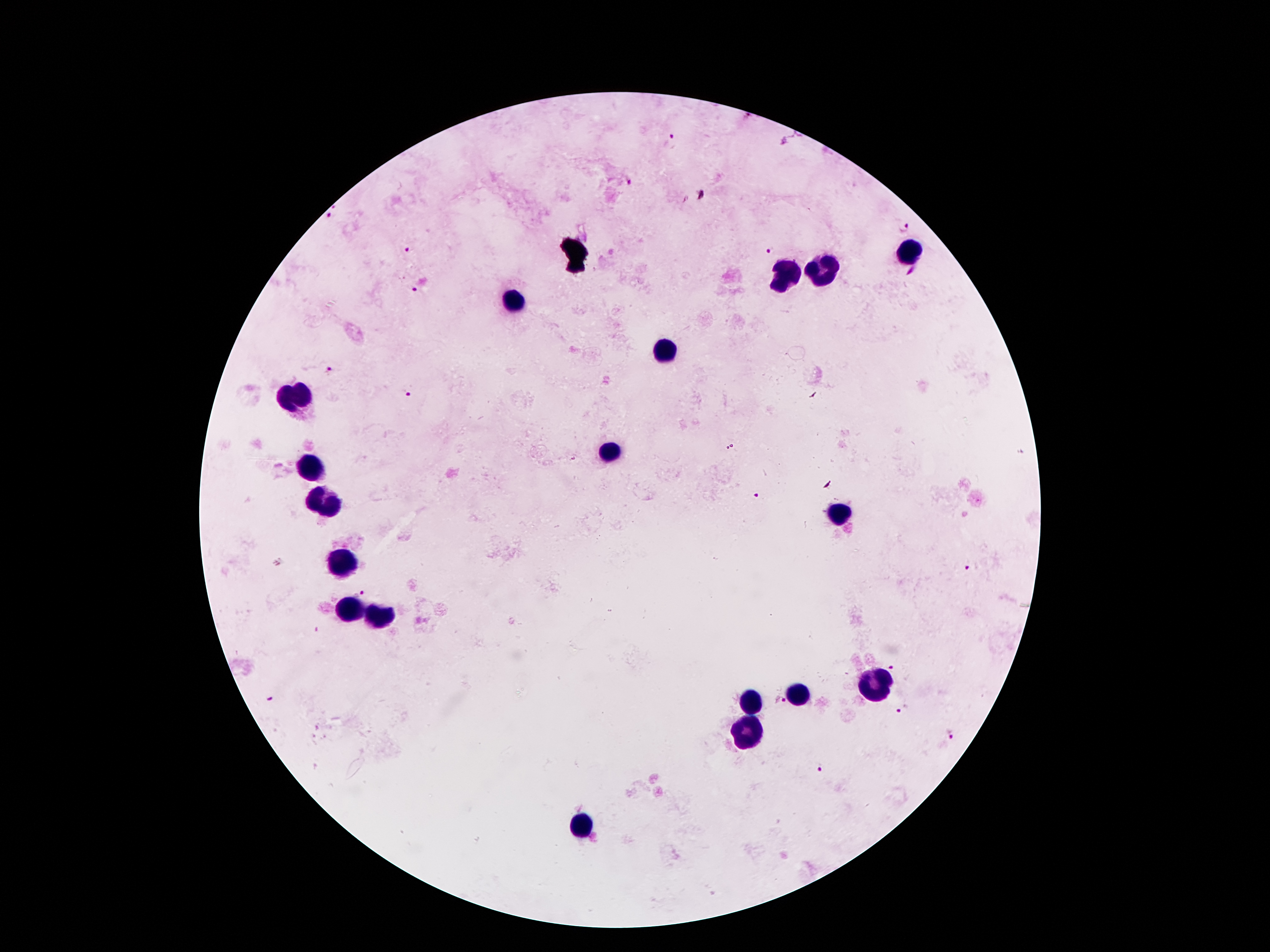

image_size: 1270×952 pixels
leukocyte_locations: 'approximate centers as [x, y] in pixels: [905, 250], [823, 272], [787, 275], [515, 298], [668, 349], [298, 398], [607, 451], [314, 469], [327, 504], [843, 513], [344, 564], [350, 609], [382, 614], [879, 688], [797, 696], [752, 705], [749, 734], [584, 826]'
preparation: thick peripheral-blood smear
capture: smartphone through the microscope eyepiece
magnification: 100x
field_of_view: one from this slide
patient_malaria_status: infected with Plasmodium falciparum
plasmodium_parasite_locations: 'approximate centers as [x, y] in pixels: [672, 141], [332, 215], [905, 227], [407, 249], [768, 249], [411, 289], [329, 367], [407, 394], [755, 496], [971, 568], [361, 590], [893, 666], [779, 701], [902, 710], [953, 734], [820, 768]'
stain: Giemsa